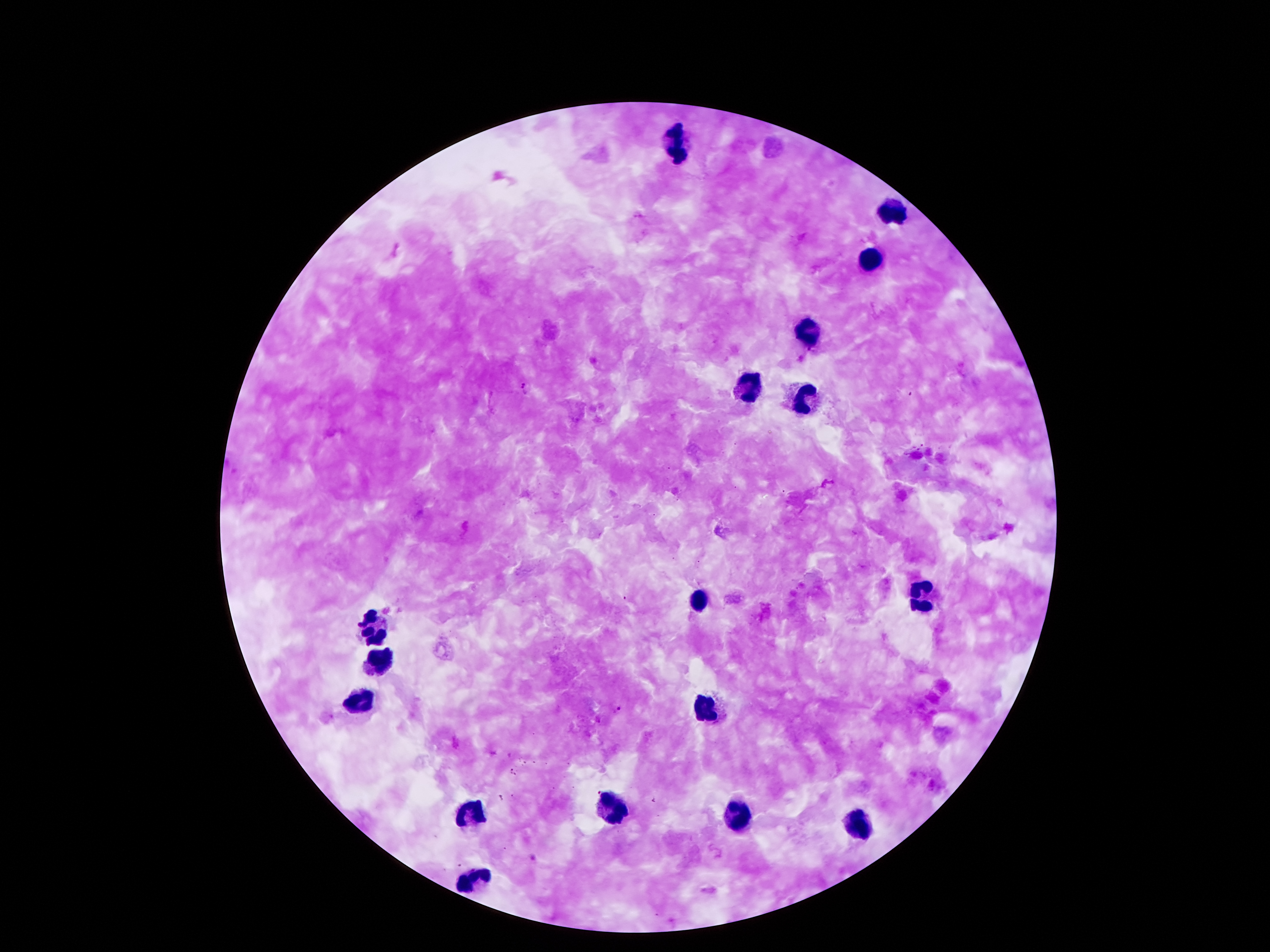
Approximate centers as [x, y] in pixels. Leukocyte locations: [678, 148], [888, 210], [868, 262], [804, 333], [745, 390], [807, 399], [920, 593], [698, 600], [374, 629], [379, 662], [357, 701], [705, 708], [611, 805], [475, 811], [740, 820], [858, 823], [473, 880]. Plasmodium parasite locations: [525, 387], [619, 709]. Giemsa-stained preparation. Single field of view. Image is 1270×952 pixels. Photographed through the microscope eyepiece with a smartphone camera. 100x magnification. Patient malaria status: infected with Plasmodium falciparum. Thick blood film.